Report the malaria status of this cell.
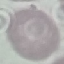

Uninfected.

Summary:
  - Stain: Giemsa
  - Preparation: thin blood film
  - Capture: smartphone camera at the microscope eyepiece
  - Image type: cell patch, automatically extracted from a larger field of view and resized to 64 × 64 pixels